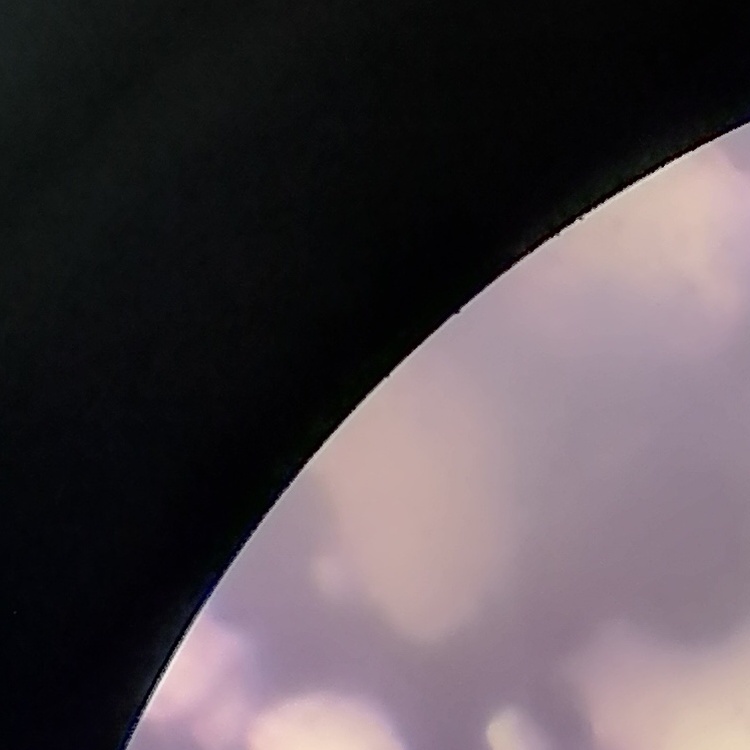 The erythrocytes exhibit rouleaux formation. Stained with either Field's or Giemsa. One tile cut from a larger photomicrograph. Thin blood smear.